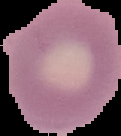
Cell region segmented out of the field of view; the surrounding area is masked to black. Result: no Plasmodium parasites detected. Image is 121×136 pixels. From a thin blood smear.